State which parasite is depicted.
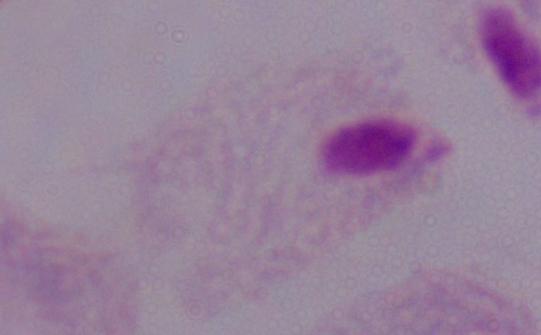

A trichomonad.

{
  "modality": "micrograph",
  "magnification": "1000x"
}